Give the position of every Plasmodium parasite visible.
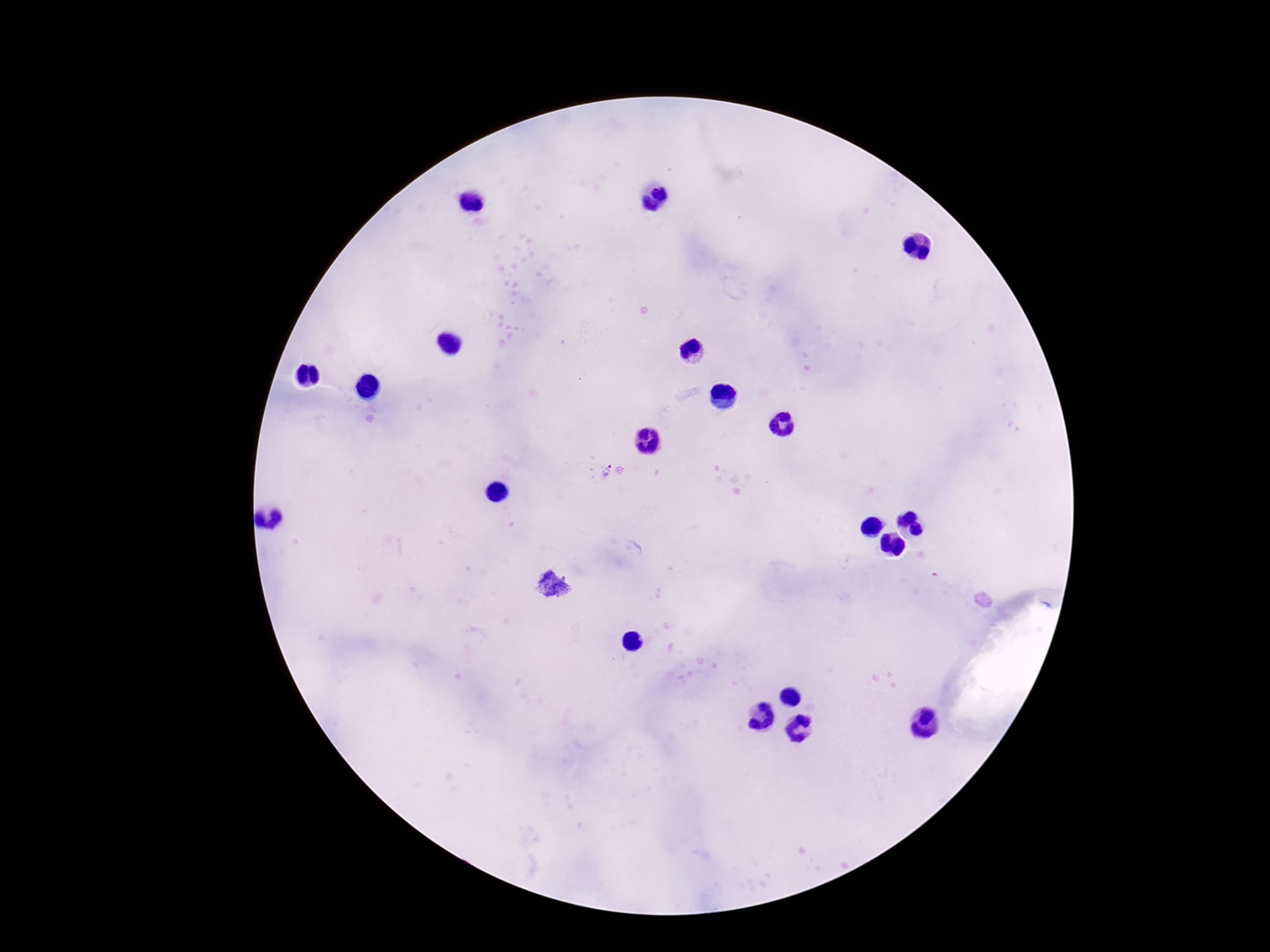
Approximate object centers, in pixels from the top-left corner.
Plasmodium parasites: (x=602, y=471), (x=553, y=586).

Patient malaria status: infected. 100x magnification. Image is 1270×952 pixels. One field from this slide. Thick blood smear. Giemsa-stained preparation. Photographed through the microscope eyepiece with a smartphone camera.